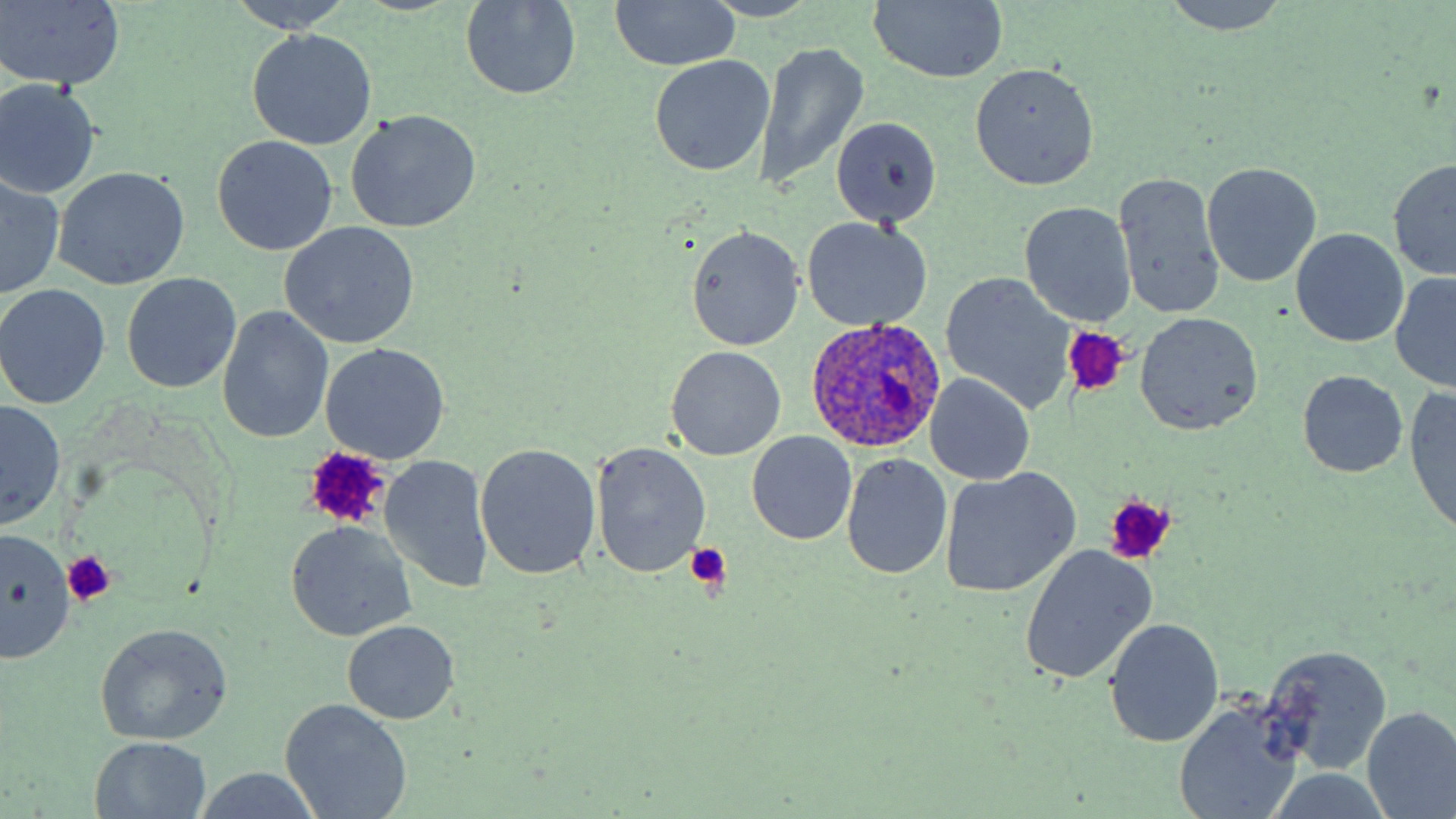 Approximate bounding boxes as (x1,y1)-(x2,y2) corner pairs in pixels. Plasmodium ovale-infected red blood cell locations: (806,316)-(946,453). Platelet locations: (1062,327)-(1129,397), (301,447)-(391,529), (1103,494)-(1177,563), (684,541)-(730,592), (63,551)-(116,605). Uninfected red blood cell locations: (225,0)-(355,32), (609,0)-(741,71), (1157,0)-(1291,34), (0,1)-(127,92), (867,1)-(1008,85), (459,2)-(581,100), (247,28)-(377,151), (754,42)-(869,189), (650,55)-(776,177), (967,62)-(1101,191), (0,78)-(102,201), (345,109)-(482,233), (830,117)-(942,227), (213,135)-(338,256), (1388,160)-(1456,282), (1202,162)-(1321,287), (53,168)-(189,290), (1114,171)-(1225,323), (1,176)-(63,300), (1020,202)-(1137,327), (800,216)-(932,331), (280,222)-(420,349), (685,227)-(804,350), (1292,230)-(1407,348), (941,272)-(1075,412), (122,273)-(242,394), (1390,274)-(1456,391), (0,286)-(110,408), (218,306)-(335,443), (1136,312)-(1261,432), (321,343)-(449,464), (666,346)-(786,462), (1296,370)-(1408,477), (926,374)-(1035,486), (1407,386)-(1456,533), (1,400)-(65,531), (748,432)-(857,543), (590,442)-(711,579), (475,444)-(601,580), (842,453)-(951,580), (378,455)-(494,594), (942,468)-(1079,597), (285,521)-(416,641), (0,529)-(75,662), (1020,545)-(1155,684), (1104,618)-(1225,748), (344,621)-(458,724), (95,623)-(233,745), (1261,643)-(1392,777), (281,699)-(413,819), (1175,704)-(1301,819), (1362,706)-(1456,818), (89,736)-(212,819), (191,771)-(327,819). Slide-level diagnosis: Plasmodium ovale. Optical microscopy. Image is 1456×819 pixels. Thin blood film. May-Grünwald-Giemsa stain. Single field of view. Captured at 1000x magnification.